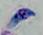
Summary:
  - Modality: micrograph
  - Magnification: 1000x
  - Identification: Toxoplasma gondii